Assess this cell for malaria.
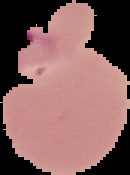
Parasitized.

Summary:
  - Image type: segmented cell region with the area outside set to black
  - Preparation: thin blood smear
  - Image size: 130×175 pixels